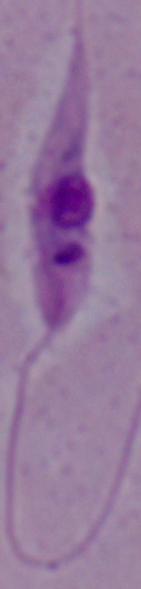

Summary:
  - Identification: Leishmania
  - Modality: photomicrograph
  - Magnification: 1000x